Assess this cell for malaria.
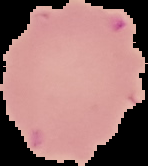
It is uninfected.

From a thin blood film. Segmented cell region on a black background. Image is 148×166 pixels.